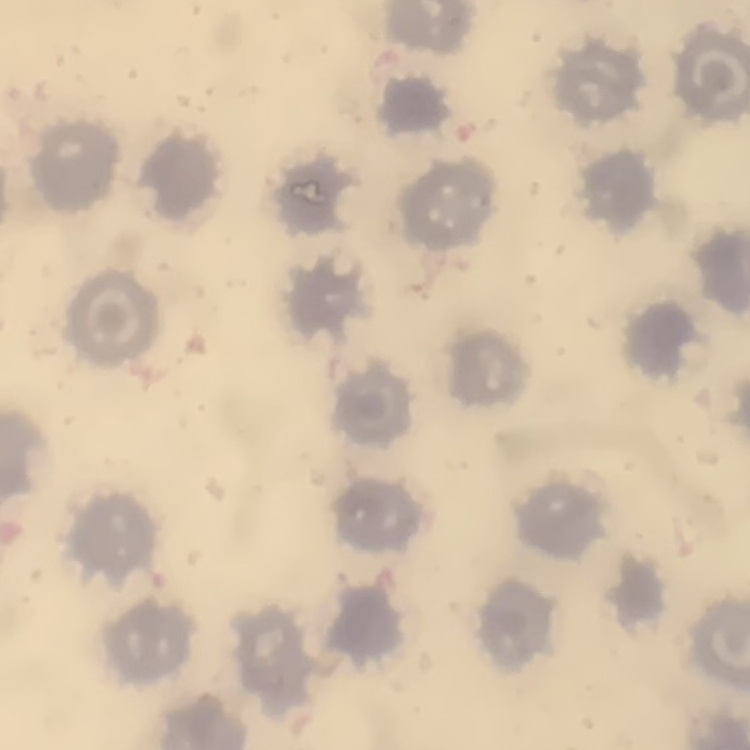 The red blood cells show no rouleaux formation. Stained with either Field's or Giemsa. One tile cut from a larger photomicrograph. Thin peripheral smear.